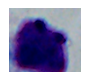

Summary:
  - Modality: micrograph
  - Magnification: 1000x
  - Identification: white blood cell